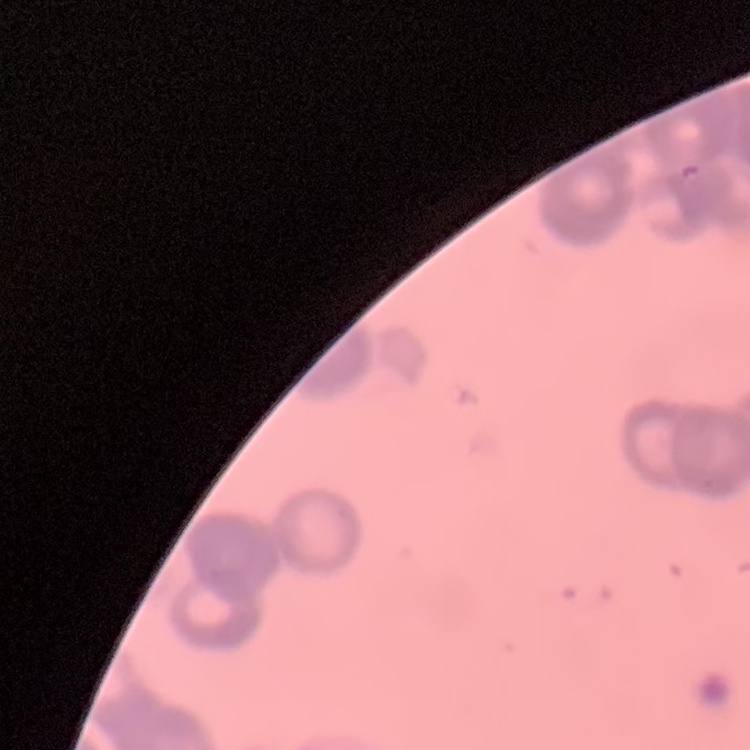
red blood cell morphology = rouleaux formation
image type = square crop of a larger photomicrograph
stain = Field's or Giemsa
preparation = thin blood film